Assess the morphology of the erythrocytes.
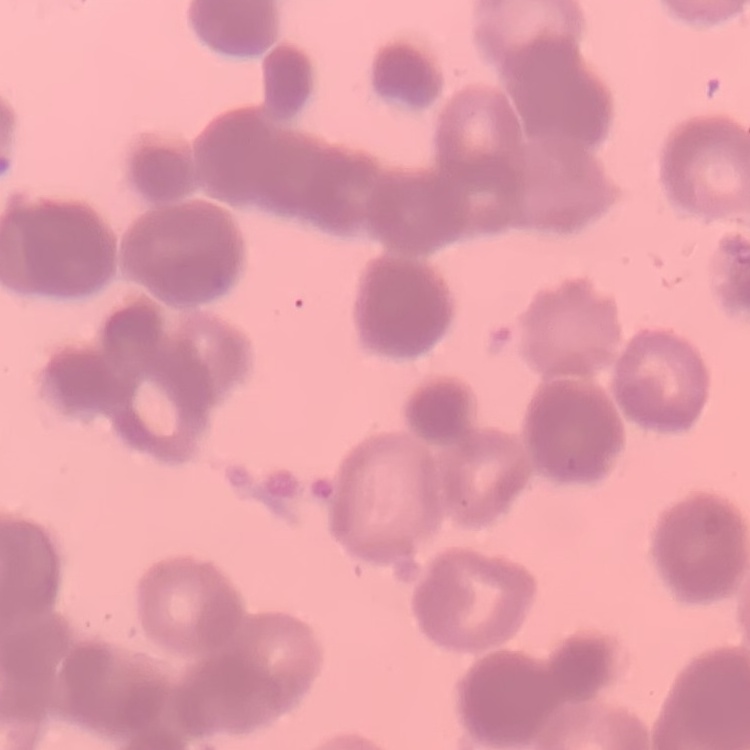

They show rouleaux formation.

Square crop of a larger photomicrograph. Stained with either Field's or Giemsa. Thin blood film.